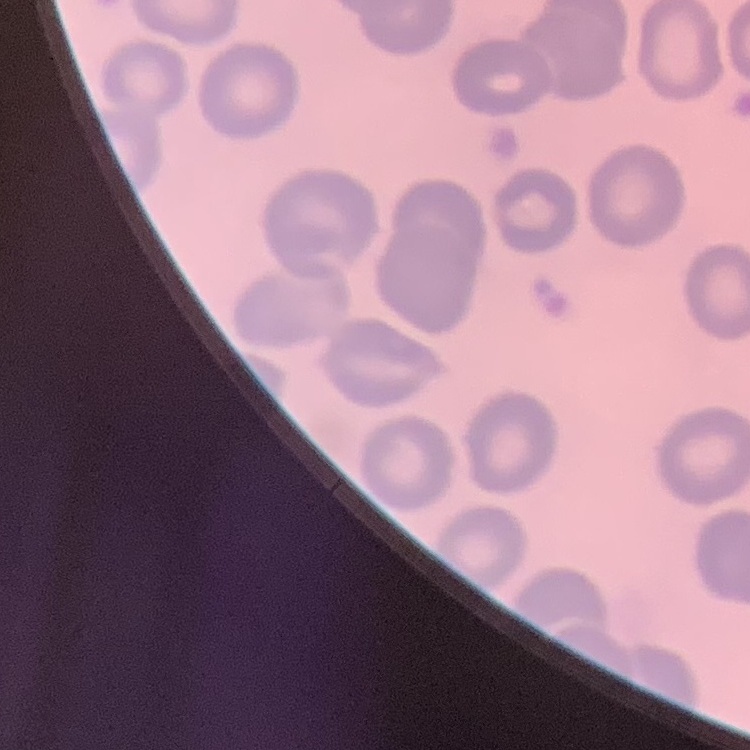

The erythrocytes show no rouleaux formation. Stained with either Field's or Giemsa. One tile cut from a larger photomicrograph. Thin blood film.